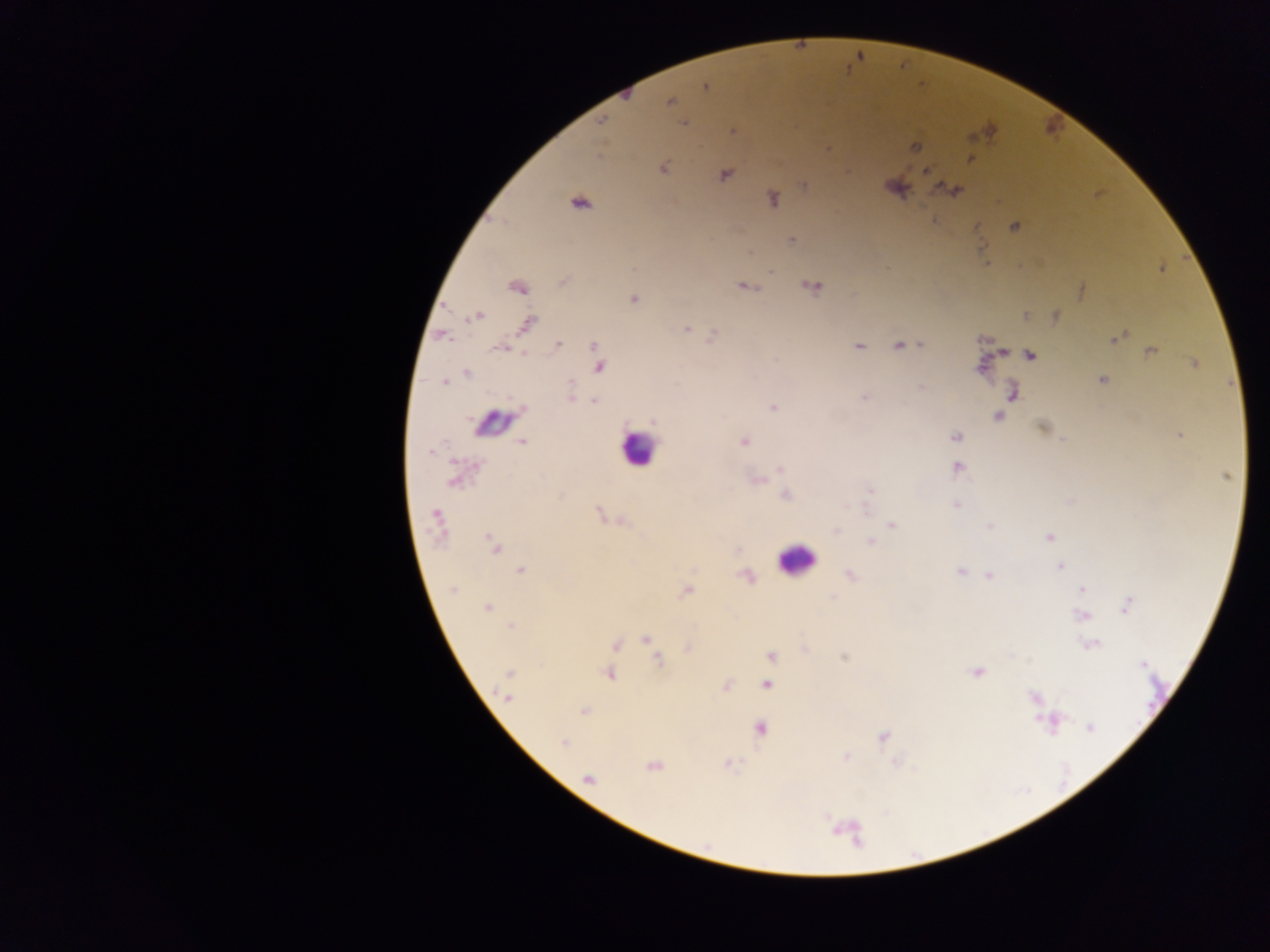 Approximate centers as [x, y] in pixels. Leukocyte locations: [486, 421], [636, 449], [795, 559]. Plasmodium parasite locations: [706, 86], [670, 102], [602, 120], [683, 124], [734, 131], [916, 147], [970, 160], [663, 168], [927, 172], [725, 175], [803, 184], [953, 190], [773, 199], [580, 203], [1014, 227], [791, 240], [1162, 269], [811, 286], [516, 287], [745, 287], [1081, 291], [633, 299], [476, 316], [1026, 316], [1056, 317], [527, 324], [686, 330], [1119, 336], [559, 344], [594, 345], [899, 346], [859, 347], [499, 349], [1151, 351], [1004, 352], [1030, 355], [1194, 364], [600, 367], [981, 367], [466, 373], [1102, 380], [445, 382], [1013, 392], [864, 397], [571, 398], [594, 401], [773, 408], [997, 416], [1042, 428], [1179, 435], [956, 437], [522, 442], [743, 442], [430, 452], [780, 468], [957, 468], [1227, 476], [452, 482], [870, 491], [785, 496], [956, 505], [598, 511], [435, 515], [892, 525], [989, 526], [835, 530], [1048, 538], [870, 542], [493, 543], [1059, 566], [521, 570], [959, 572], [851, 575], [988, 576], [1082, 589], [453, 590], [686, 591], [1127, 605], [486, 607], [1081, 615], [510, 626], [647, 639], [1091, 644], [616, 645], [687, 648], [771, 656], [845, 656], [658, 660], [1142, 664], [977, 672], [509, 674], [609, 674], [767, 685], [727, 686], [1034, 697], [507, 698], [583, 711], [1053, 722], [1090, 727], [760, 728], [883, 737], [564, 744], [846, 758], [651, 766], [588, 779]. Photographed through a microscope with a mobile-phone camera. Collected in Ghana. Image is 1270×952 pixels. Thick blood film. Single field of view.